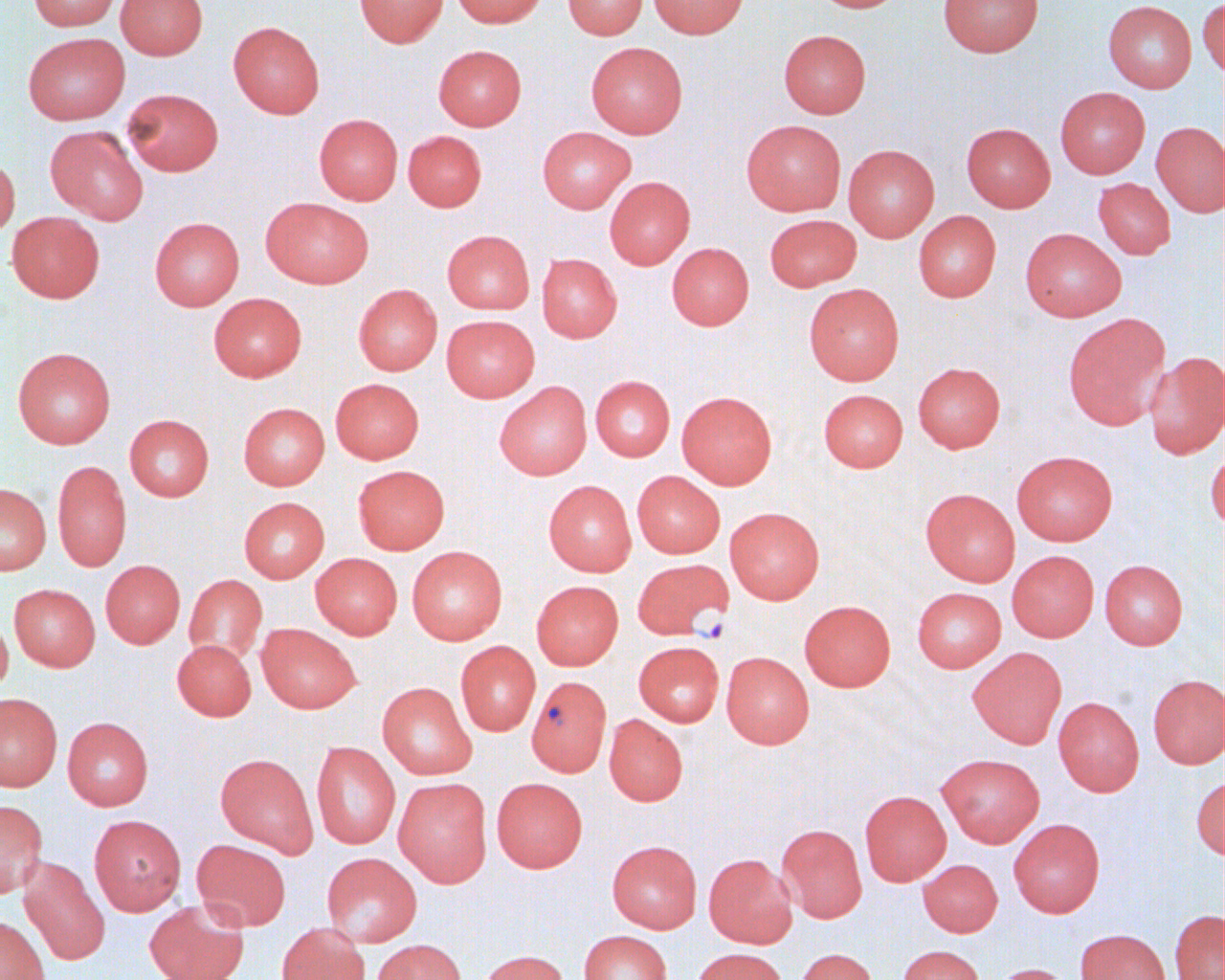
Approximate bounding boxes as [x1, y1, x2, y2] in pixels. Plasmodium falciparum-infected red blood cell locations: [637, 563, 738, 644], [526, 675, 611, 777]. Uninfected red blood cell locations: [29, 0, 120, 31], [115, 0, 208, 60], [354, 0, 449, 48], [451, 0, 547, 28], [563, 0, 648, 39], [648, 0, 749, 38], [812, 0, 909, 13], [937, 0, 1044, 57], [1197, 0, 1224, 79], [1103, 1, 1197, 92], [228, 21, 325, 118], [778, 29, 871, 118], [23, 32, 130, 124], [586, 42, 688, 138], [433, 45, 527, 130], [1055, 87, 1150, 178], [122, 88, 224, 175], [314, 113, 403, 205], [741, 119, 846, 216], [1151, 121, 1225, 217], [961, 122, 1056, 212], [45, 125, 148, 225], [537, 127, 635, 213], [403, 131, 487, 211], [843, 144, 939, 242], [0, 156, 20, 239], [604, 176, 695, 269], [1093, 178, 1176, 259], [261, 197, 374, 288], [913, 211, 1001, 302], [6, 212, 105, 303], [764, 214, 862, 292], [149, 217, 244, 311], [1020, 227, 1126, 321], [442, 230, 535, 314], [667, 242, 754, 330], [537, 253, 622, 343], [804, 283, 904, 385], [353, 284, 443, 375], [208, 293, 306, 382], [1062, 312, 1171, 430], [441, 315, 540, 402], [12, 347, 116, 449], [1143, 351, 1225, 460], [912, 362, 1006, 452], [590, 375, 675, 461], [330, 378, 424, 464], [494, 381, 592, 480], [818, 389, 908, 472], [677, 391, 777, 489], [238, 402, 330, 490], [124, 414, 214, 501], [1206, 445, 1225, 532], [1011, 450, 1118, 545], [52, 460, 131, 572], [352, 465, 449, 554], [632, 470, 725, 558], [543, 480, 636, 576], [0, 483, 51, 574], [920, 488, 1020, 586], [239, 497, 330, 583], [724, 506, 825, 604], [406, 546, 507, 645], [1007, 550, 1099, 642], [310, 553, 402, 639], [1099, 559, 1188, 649], [100, 560, 185, 649], [184, 574, 267, 664], [531, 580, 623, 670], [9, 584, 100, 671], [912, 587, 1005, 672], [799, 600, 896, 691], [0, 614, 13, 695], [256, 623, 361, 713], [172, 639, 256, 721], [455, 641, 541, 736], [633, 641, 724, 727], [967, 646, 1067, 748], [721, 651, 814, 749], [1147, 674, 1225, 769], [377, 682, 477, 780], [0, 693, 62, 791], [1053, 696, 1144, 796], [603, 714, 688, 806], [62, 717, 153, 811], [311, 741, 400, 849], [215, 753, 319, 857], [936, 753, 1045, 847], [1191, 774, 1225, 861], [393, 777, 492, 887], [491, 777, 588, 872], [859, 790, 952, 886], [0, 800, 47, 898], [88, 814, 186, 916], [1008, 818, 1105, 917], [776, 823, 868, 923], [191, 839, 291, 931], [607, 840, 702, 933], [321, 852, 422, 947], [703, 853, 797, 948], [18, 855, 110, 966], [917, 859, 1003, 937], [144, 900, 249, 980], [1169, 909, 1224, 980], [0, 914, 49, 980], [277, 922, 369, 980], [1075, 928, 1171, 980], [579, 930, 672, 980], [371, 938, 466, 980], [897, 945, 984, 980], [691, 947, 788, 980], [794, 948, 878, 980], [475, 949, 569, 980], [991, 963, 1075, 980]. Slide-level diagnosis: Plasmodium falciparum. Thin blood film. Image is 1225×980 pixels. 1000x magnification. Light microscopy. One field of a larger specimen.